Report the malaria status of this cell.
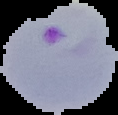
Parasitized.

Image is 118×115 pixels. The area outside the segmented cell region is set to black. From a thin blood smear.